Report the malaria status of this cell.
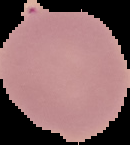
Uninfected.

{
  "image_type": "segmented cell region on a black background",
  "preparation": "thin blood film",
  "image_size": "130×145 pixels"
}